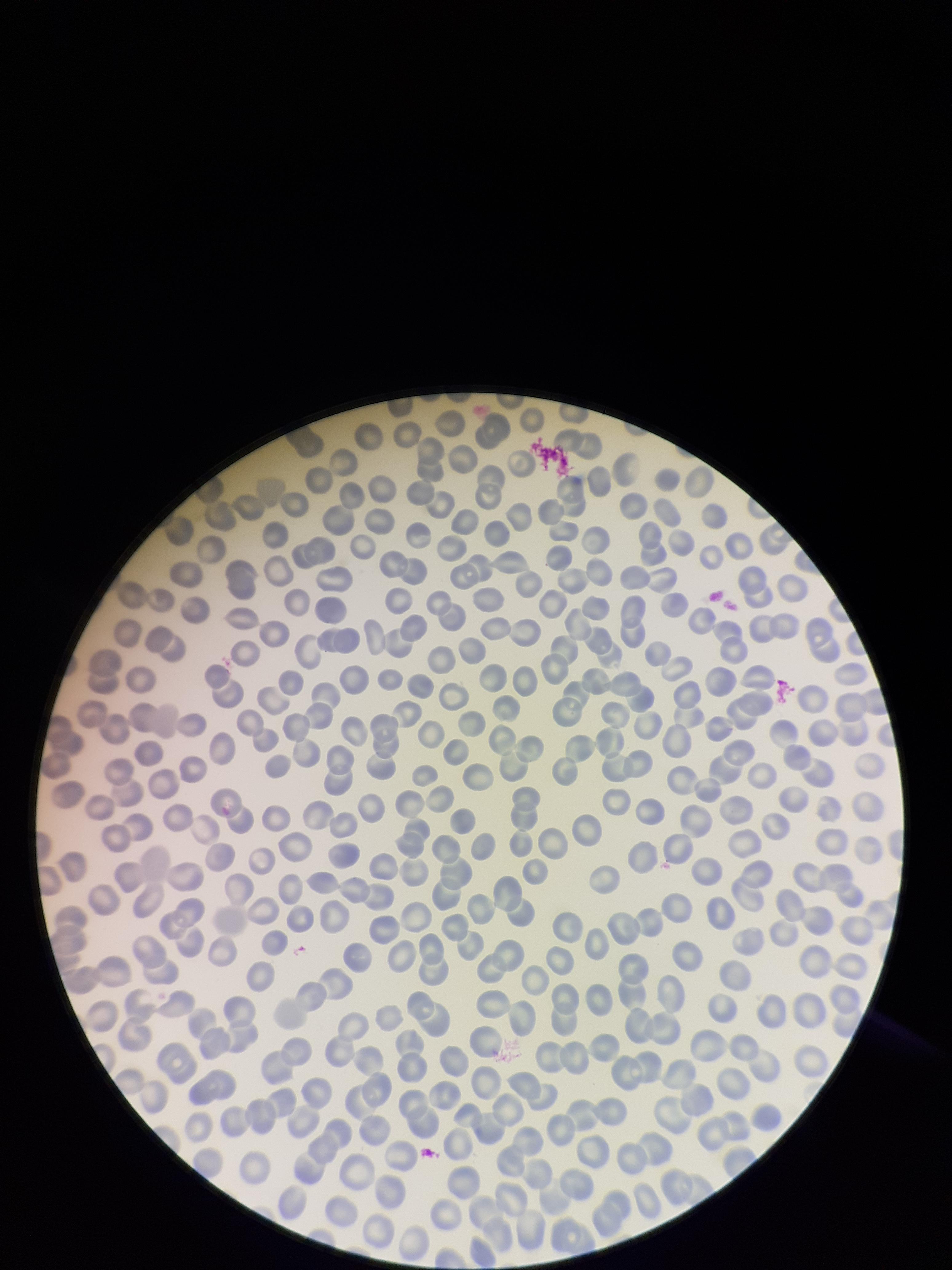

{
  "image_size": "952×1270 pixels",
  "parasitized_red_blood_cells": "none identified",
  "stain": "Giemsa",
  "patient_malaria_status": "negative",
  "parasitized_red_blood_cell_count": 0,
  "capture": "smartphone photograph through the microscope eyepiece",
  "preparation": "thin blood smear",
  "red_blood_cell_count": 310,
  "field_of_view": "one from this slide"
}